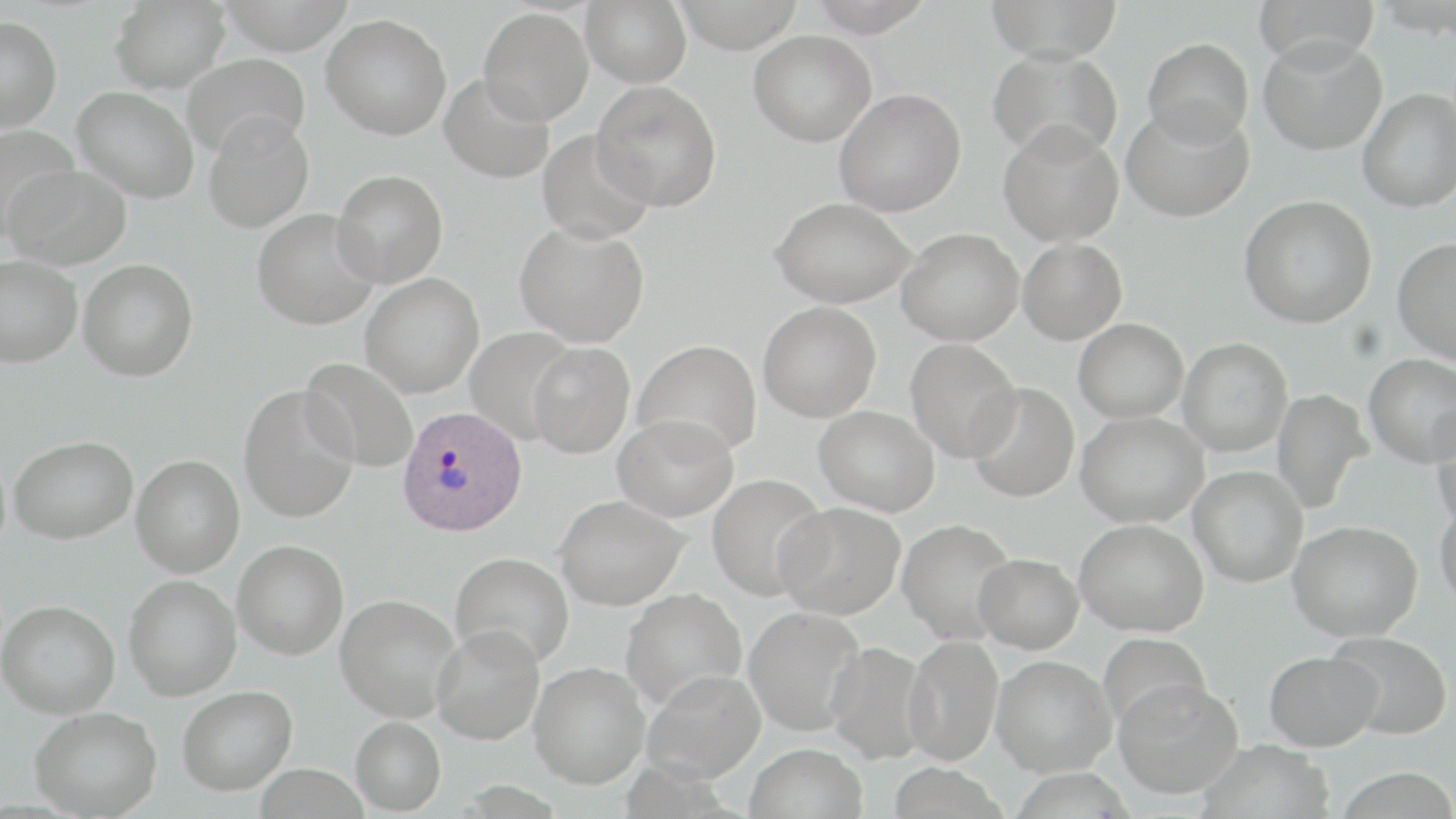
Approximate bounding boxes as named x1/y1/x2/y2 corners in pixels. Plasmodium ovale-infected red blood cell locations: (x1=395, y1=406, x2=527, y2=537). Uninfected red blood cell locations: (x1=110, y1=0, x2=231, y2=93), (x1=581, y1=0, x2=691, y2=87), (x1=671, y1=0, x2=805, y2=53), (x1=804, y1=0, x2=935, y2=36), (x1=984, y1=0, x2=1124, y2=61), (x1=1253, y1=0, x2=1380, y2=67), (x1=478, y1=7, x2=593, y2=125), (x1=321, y1=13, x2=451, y2=140), (x1=0, y1=16, x2=62, y2=132), (x1=749, y1=30, x2=877, y2=146), (x1=1258, y1=35, x2=1386, y2=155), (x1=1142, y1=37, x2=1253, y2=146), (x1=987, y1=48, x2=1123, y2=162), (x1=181, y1=52, x2=309, y2=158), (x1=440, y1=73, x2=554, y2=184), (x1=591, y1=81, x2=722, y2=211), (x1=72, y1=86, x2=199, y2=203), (x1=834, y1=88, x2=966, y2=217), (x1=1357, y1=88, x2=1456, y2=212), (x1=1121, y1=103, x2=1254, y2=222), (x1=203, y1=112, x2=315, y2=233), (x1=998, y1=119, x2=1125, y2=246), (x1=0, y1=124, x2=80, y2=243), (x1=536, y1=129, x2=654, y2=244), (x1=4, y1=163, x2=133, y2=271), (x1=332, y1=169, x2=448, y2=287), (x1=1239, y1=195, x2=1377, y2=328), (x1=770, y1=196, x2=916, y2=307), (x1=252, y1=208, x2=381, y2=330), (x1=514, y1=221, x2=650, y2=347), (x1=896, y1=228, x2=1024, y2=346), (x1=1018, y1=237, x2=1128, y2=344), (x1=1393, y1=237, x2=1456, y2=365), (x1=0, y1=254, x2=83, y2=367), (x1=78, y1=259, x2=198, y2=381), (x1=360, y1=273, x2=484, y2=397), (x1=758, y1=301, x2=881, y2=422), (x1=1073, y1=318, x2=1189, y2=423), (x1=465, y1=328, x2=579, y2=444), (x1=1178, y1=337, x2=1293, y2=457), (x1=906, y1=338, x2=1021, y2=462), (x1=632, y1=340, x2=763, y2=458), (x1=527, y1=342, x2=635, y2=458), (x1=1364, y1=353, x2=1456, y2=466), (x1=300, y1=358, x2=419, y2=472), (x1=967, y1=382, x2=1080, y2=503), (x1=238, y1=384, x2=360, y2=523), (x1=1271, y1=388, x2=1372, y2=515), (x1=814, y1=405, x2=940, y2=517), (x1=1430, y1=408, x2=1456, y2=526), (x1=1076, y1=411, x2=1208, y2=527), (x1=613, y1=414, x2=738, y2=522), (x1=9, y1=435, x2=137, y2=544), (x1=132, y1=455, x2=245, y2=577), (x1=1189, y1=466, x2=1308, y2=587), (x1=707, y1=473, x2=829, y2=601), (x1=555, y1=494, x2=688, y2=610), (x1=1434, y1=498, x2=1456, y2=608), (x1=774, y1=501, x2=906, y2=619), (x1=897, y1=518, x2=1018, y2=644), (x1=1075, y1=518, x2=1209, y2=637), (x1=1288, y1=520, x2=1422, y2=641), (x1=233, y1=540, x2=349, y2=660), (x1=450, y1=552, x2=574, y2=668), (x1=974, y1=553, x2=1084, y2=653), (x1=124, y1=575, x2=242, y2=700), (x1=620, y1=588, x2=747, y2=711), (x1=336, y1=593, x2=461, y2=722), (x1=0, y1=599, x2=120, y2=718), (x1=743, y1=606, x2=865, y2=736), (x1=431, y1=625, x2=546, y2=745), (x1=1326, y1=631, x2=1453, y2=739), (x1=1097, y1=632, x2=1211, y2=732), (x1=903, y1=634, x2=1003, y2=766), (x1=824, y1=640, x2=929, y2=764), (x1=1264, y1=650, x2=1382, y2=750), (x1=991, y1=655, x2=1116, y2=776), (x1=529, y1=661, x2=649, y2=788), (x1=642, y1=669, x2=766, y2=783), (x1=1114, y1=678, x2=1243, y2=799), (x1=177, y1=685, x2=297, y2=795), (x1=30, y1=705, x2=162, y2=818), (x1=350, y1=716, x2=446, y2=815), (x1=1197, y1=740, x2=1335, y2=819), (x1=744, y1=742, x2=868, y2=819), (x1=888, y1=764, x2=1008, y2=819), (x1=1332, y1=767, x2=1456, y2=819). Slide-level diagnosis: Plasmodium ovale. Thin blood film. Image is 1456×819 pixels. May-Grünwald-Giemsa-stained preparation. 1000x magnification. Light microscopy. Single field of view.